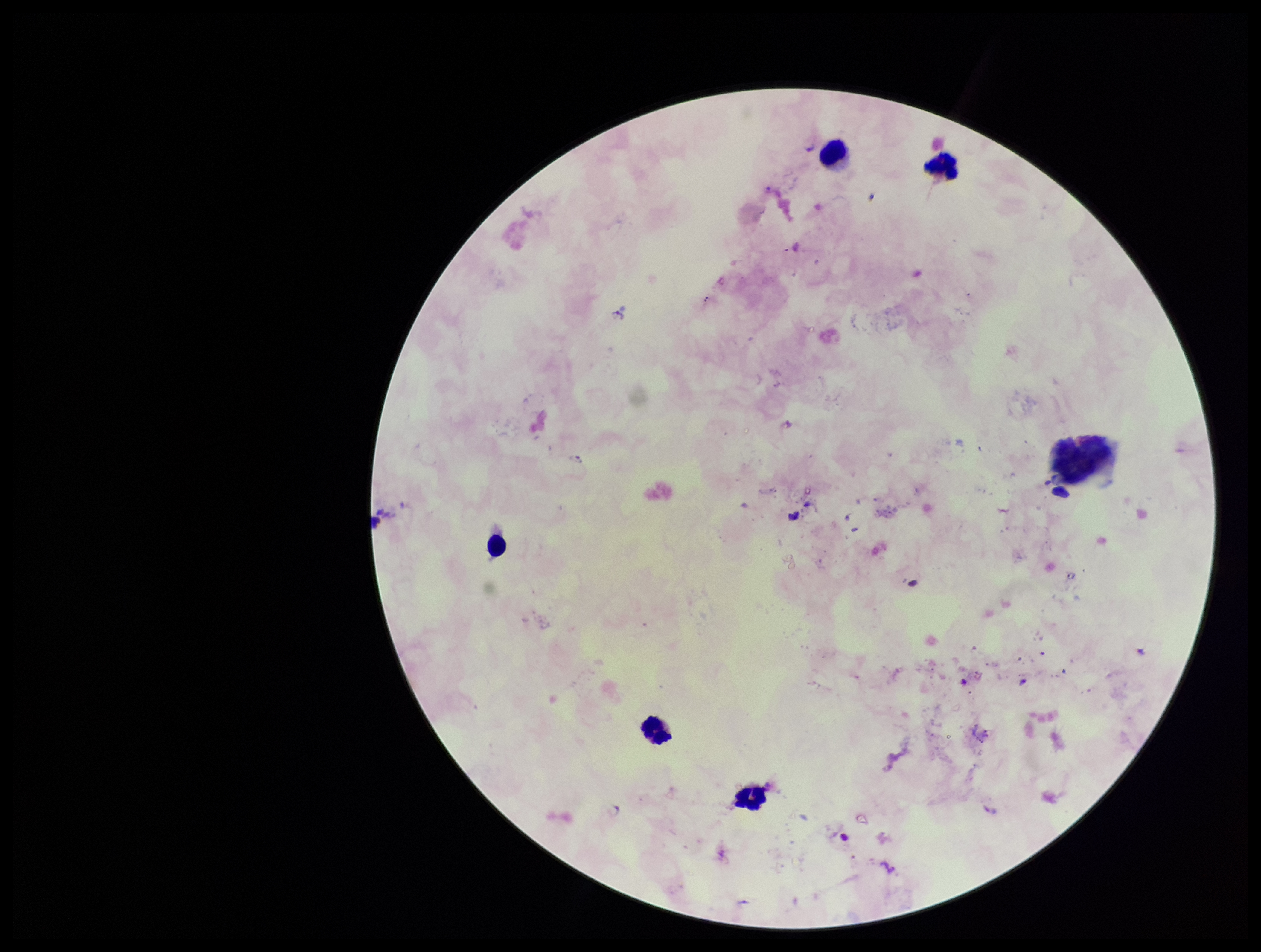
{
  "patient_malaria_status": "infected",
  "species_reported_for_this_patient": "Plasmodium falciparum",
  "field_of_view": "one from this slide",
  "leukocyte_count": 6,
  "image_size": "1261×952 pixels",
  "plasmodium_parasites": "identified",
  "stain": "Giemsa",
  "parasite_count": 2,
  "capture": "smartphone photograph through the microscope eyepiece",
  "preparation": "thick"
}